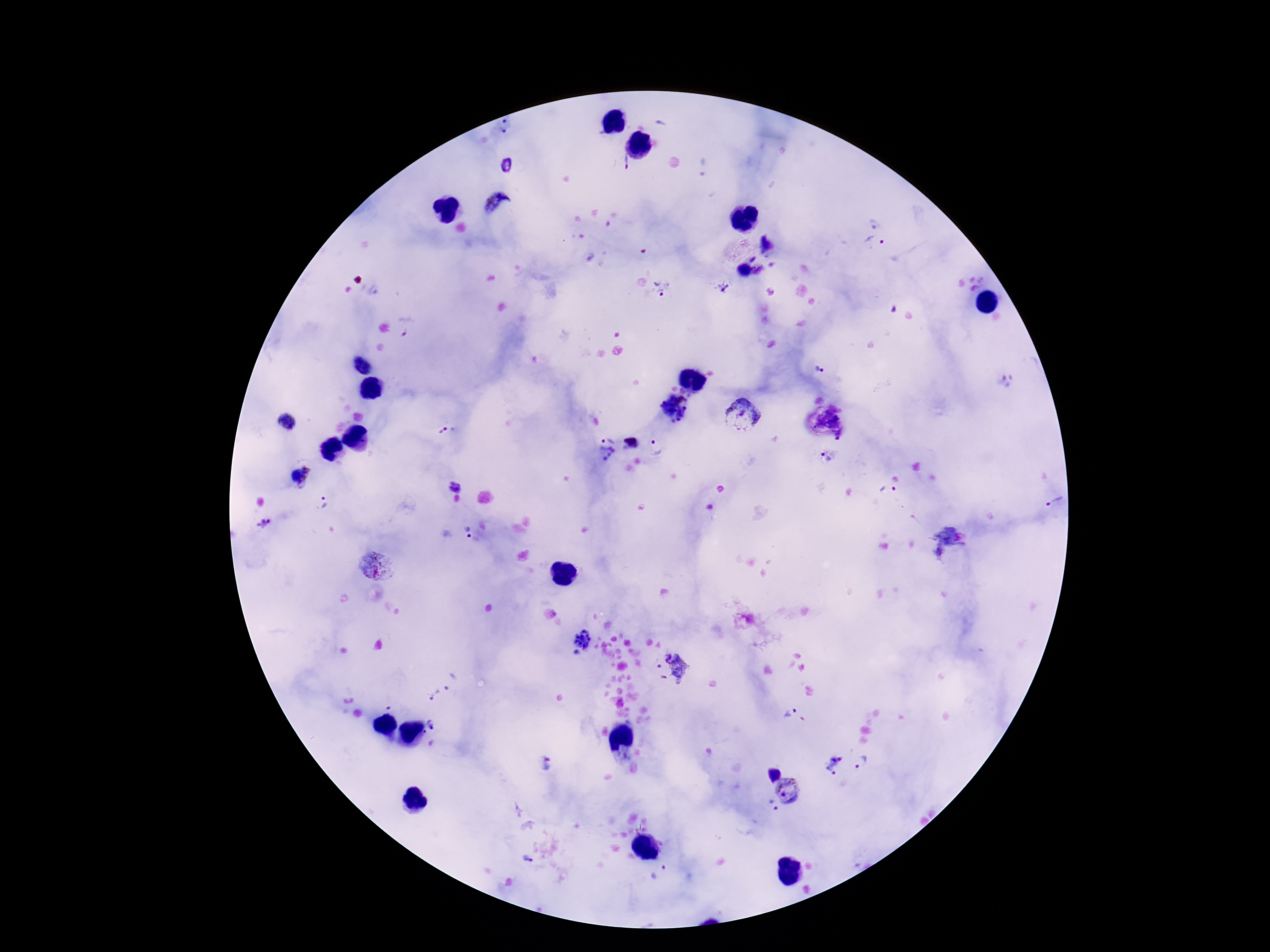
image size = 1270×952 pixels
capture = smartphone camera through the microscope eyepiece
preparation = thick peripheral-blood smear
Plasmodium parasite locations = approximate centers as [x, y] in pixels: [505, 127], [625, 163], [506, 166], [498, 206], [875, 242], [758, 269], [719, 286], [662, 289], [407, 326], [361, 366], [820, 371], [1008, 382], [676, 409], [743, 414], [287, 423], [441, 430], [629, 442], [656, 447], [606, 450], [827, 456], [308, 469], [303, 484], [454, 485], [888, 494], [324, 502], [1054, 502], [263, 524], [468, 533], [376, 564], [580, 641], [674, 672], [452, 682], [433, 694], [389, 708], [790, 712], [432, 725], [544, 762], [862, 762], [833, 764], [774, 773], [791, 792], [771, 808], [527, 860]
field of view = one from this slide
stain = Giemsa
magnification = 100x
patient malaria status = positive